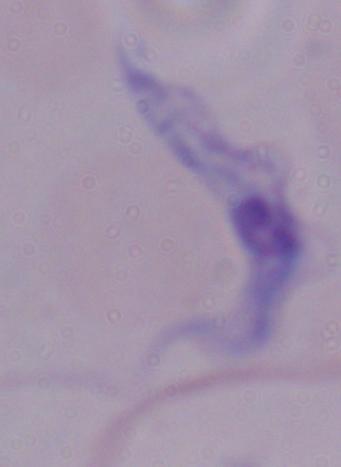
modality: micrograph
magnification: 1000x
identification: trypanosome